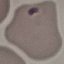 Result: malaria parasites detected. Automatically extracted cell patch, resized to 64 × 64 pixels. Giemsa-stained preparation. Photographed with a smartphone camera at the microscope eyepiece. Thin smear of blood.